Outline each blood parasite and name the species.
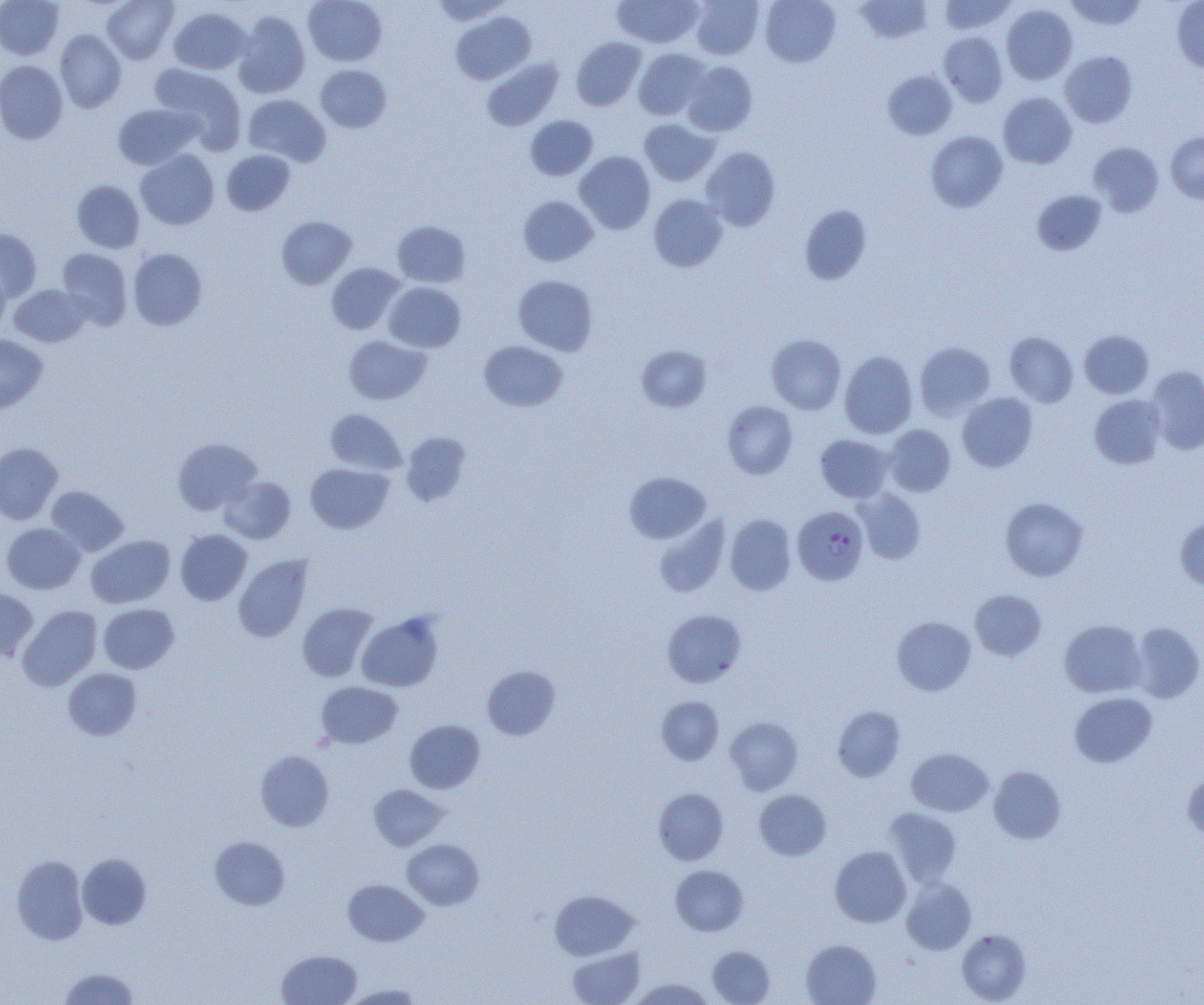

Approximate bounding boxes as (x1, y1, x2, y2) in pixels.
Plasmodium falciparum-infected red blood cells: (793, 506, 868, 585).
No Plasmodium ovale, Plasmodium malariae, Plasmodium vivax, Babesia divergens, or Trypanosoma brucei observed.

Uninfected red blood cell locations: (0, 0, 64, 59), (102, 0, 179, 64), (303, 0, 387, 66), (429, 0, 512, 25), (690, 0, 764, 59), (760, 0, 841, 67), (854, 0, 934, 43), (939, 0, 1015, 34), (1064, 0, 1148, 31), (613, 1, 703, 48), (1172, 1, 1204, 74), (1001, 4, 1078, 84), (169, 7, 251, 74), (233, 11, 310, 98), (450, 11, 536, 85), (55, 30, 126, 112), (939, 31, 1008, 106), (571, 37, 646, 110), (633, 48, 709, 120), (1061, 51, 1137, 127), (482, 58, 563, 131), (0, 60, 68, 144), (681, 61, 758, 136), (151, 63, 245, 149), (316, 65, 391, 132), (883, 70, 957, 140), (998, 92, 1077, 168), (243, 94, 331, 166), (113, 103, 199, 169), (526, 115, 598, 180), (639, 118, 720, 186), (926, 131, 1008, 212), (1166, 132, 1204, 204), (1088, 141, 1164, 216), (701, 146, 781, 231), (221, 149, 295, 215), (136, 150, 219, 230), (574, 151, 656, 234), (71, 180, 145, 252), (1032, 189, 1107, 255), (648, 194, 728, 272), (518, 195, 598, 266), (799, 204, 872, 285), (276, 215, 357, 289), (392, 220, 471, 287), (0, 228, 42, 301), (56, 248, 132, 329), (128, 248, 208, 331), (326, 262, 405, 334), (0, 265, 11, 335), (513, 275, 598, 355), (384, 281, 466, 352), (9, 284, 91, 347), (1079, 329, 1154, 398), (1004, 331, 1078, 406), (0, 334, 48, 413), (766, 334, 846, 414), (344, 335, 431, 404), (479, 340, 568, 412), (914, 341, 996, 420), (636, 344, 711, 412), (839, 350, 917, 438), (1145, 365, 1204, 455), (957, 392, 1037, 472), (1089, 394, 1167, 469), (722, 400, 798, 479), (325, 408, 406, 475), (884, 424, 956, 496), (401, 432, 471, 506), (816, 434, 893, 503), (172, 438, 262, 515), (0, 442, 62, 525), (305, 463, 394, 534), (624, 472, 711, 543), (219, 475, 296, 544), (46, 485, 129, 555), (853, 489, 926, 565), (1000, 497, 1089, 581), (725, 514, 796, 595), (653, 515, 730, 598), (1175, 518, 1204, 590), (1, 523, 85, 594), (175, 529, 252, 605), (86, 535, 175, 608), (233, 554, 312, 642), (0, 588, 38, 661), (969, 589, 1046, 661), (98, 603, 179, 673), (297, 603, 378, 682), (16, 605, 102, 691), (662, 609, 746, 688), (356, 611, 444, 692), (892, 616, 976, 695), (1059, 619, 1146, 697), (1130, 622, 1203, 703), (481, 664, 561, 740), (63, 668, 142, 740), (316, 682, 402, 748), (1069, 692, 1157, 768), (657, 696, 725, 765), (833, 706, 905, 782), (726, 716, 803, 794), (404, 720, 485, 793), (906, 748, 994, 817), (255, 750, 334, 831), (988, 766, 1066, 844), (1182, 769, 1204, 842), (368, 784, 448, 850), (654, 788, 728, 865), (754, 789, 831, 860), (884, 807, 961, 888), (209, 835, 290, 910), (401, 839, 484, 910), (830, 846, 911, 927), (77, 853, 151, 929), (11, 855, 88, 945), (671, 865, 748, 936), (901, 878, 976, 955), (343, 879, 428, 946), (550, 890, 639, 960), (956, 929, 1031, 1004), (801, 939, 881, 1005), (567, 946, 645, 1005), (708, 946, 775, 1004), (276, 950, 362, 1005), (58, 967, 139, 1004), (630, 977, 716, 1005), (343, 983, 424, 1004). Slide-level diagnosis: Plasmodium falciparum. Thin blood smear. Captured at 1000x magnification. Image is 1204×1005 pixels. Single field of view. Light microscopy.